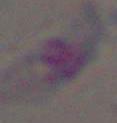

modality: photomicrograph
identification: Toxoplasma gondii
magnification: 1000x